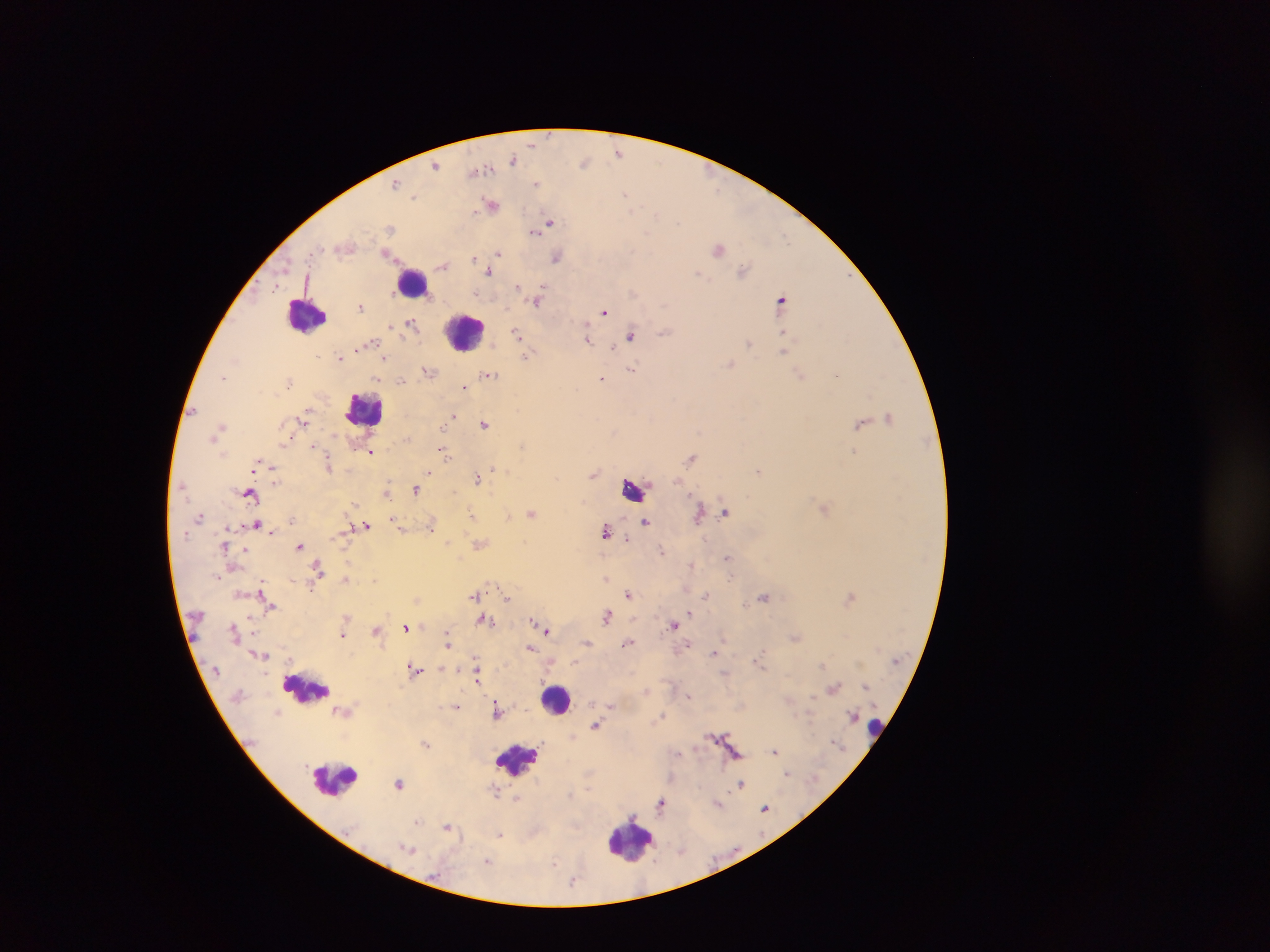
Approximate centers as (x, y) in pixels. Leukocyte locations: (413, 280), (306, 315), (464, 331), (364, 409), (632, 488), (306, 688), (556, 700), (876, 727), (516, 758), (336, 778), (629, 838). Malaria parasite locations: (532, 143), (619, 153), (514, 159), (585, 163), (436, 165), (478, 170), (396, 184), (536, 184), (626, 193), (414, 197), (491, 203), (657, 215), (549, 222), (390, 227), (534, 231), (719, 249), (388, 254), (498, 254), (474, 256), (556, 257), (442, 266), (743, 270), (490, 272), (698, 274), (518, 286), (275, 288), (476, 292), (782, 298), (538, 301), (361, 306), (605, 311), (411, 324), (391, 326), (516, 332), (664, 332), (784, 334), (631, 336), (588, 338), (749, 343), (613, 347), (784, 350), (526, 356), (236, 358), (339, 358), (385, 358), (730, 364), (631, 367), (429, 371), (488, 375), (801, 375), (836, 375), (223, 377), (601, 379), (400, 381), (464, 387), (453, 415), (889, 416), (303, 422), (484, 423), (860, 424), (220, 425), (312, 446), (522, 446), (443, 451), (853, 451), (370, 452), (691, 457), (255, 464), (328, 465), (496, 469), (507, 471), (758, 471), (429, 472), (593, 474), (477, 478), (274, 479), (415, 489), (249, 493), (386, 493), (824, 509), (726, 511), (531, 513), (471, 514), (698, 515), (508, 516), (395, 519), (645, 522), (256, 524), (366, 525), (429, 526), (400, 528), (605, 530), (271, 531), (627, 538), (225, 545), (300, 546), (245, 550), (661, 551), (727, 557), (691, 564), (318, 567), (346, 579), (262, 588), (629, 593), (475, 595), (706, 595), (763, 597), (850, 597), (507, 598), (745, 605), (271, 607), (690, 613), (607, 616), (250, 617), (484, 619), (533, 620), (674, 624), (406, 627), (376, 630), (547, 630), (447, 631), (343, 635), (795, 637), (447, 641), (587, 643), (628, 643), (531, 648), (713, 654), (823, 666), (442, 668), (415, 669), (477, 674), (865, 685), (834, 687), (689, 697), (611, 705), (457, 707), (337, 711), (497, 712), (662, 718), (596, 725), (426, 743), (775, 751), (679, 752), (787, 773), (399, 783), (741, 785), (495, 791), (517, 798), (660, 806), (765, 808), (417, 821), (448, 826), (500, 834), (407, 849), (488, 861), (555, 863), (573, 882). One field of view. Image is 1270×952 pixels. Thick blood film. Mobile-phone photograph taken through the microscope. Sample from Ghana.